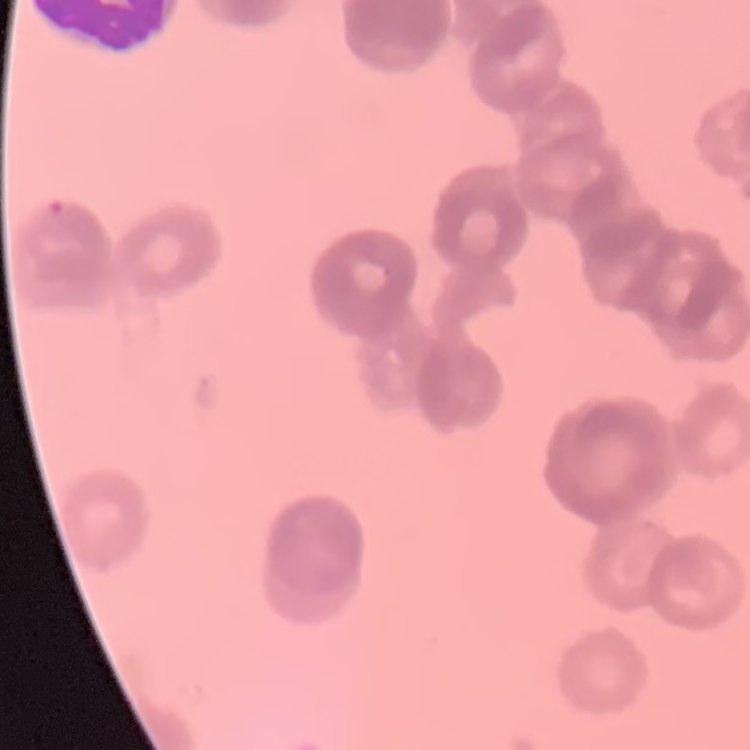

erythrocyte_morphology: rouleaux formation
image_type: square crop of a larger photomicrograph
preparation: thin blood smear
stain: Field's or Giemsa